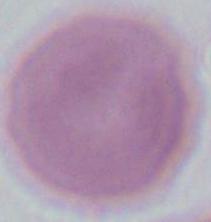

Summary:
  - Magnification: 1000x
  - Identification: red blood cell
  - Modality: photomicrograph